Locate every blood parasite and identify its species.
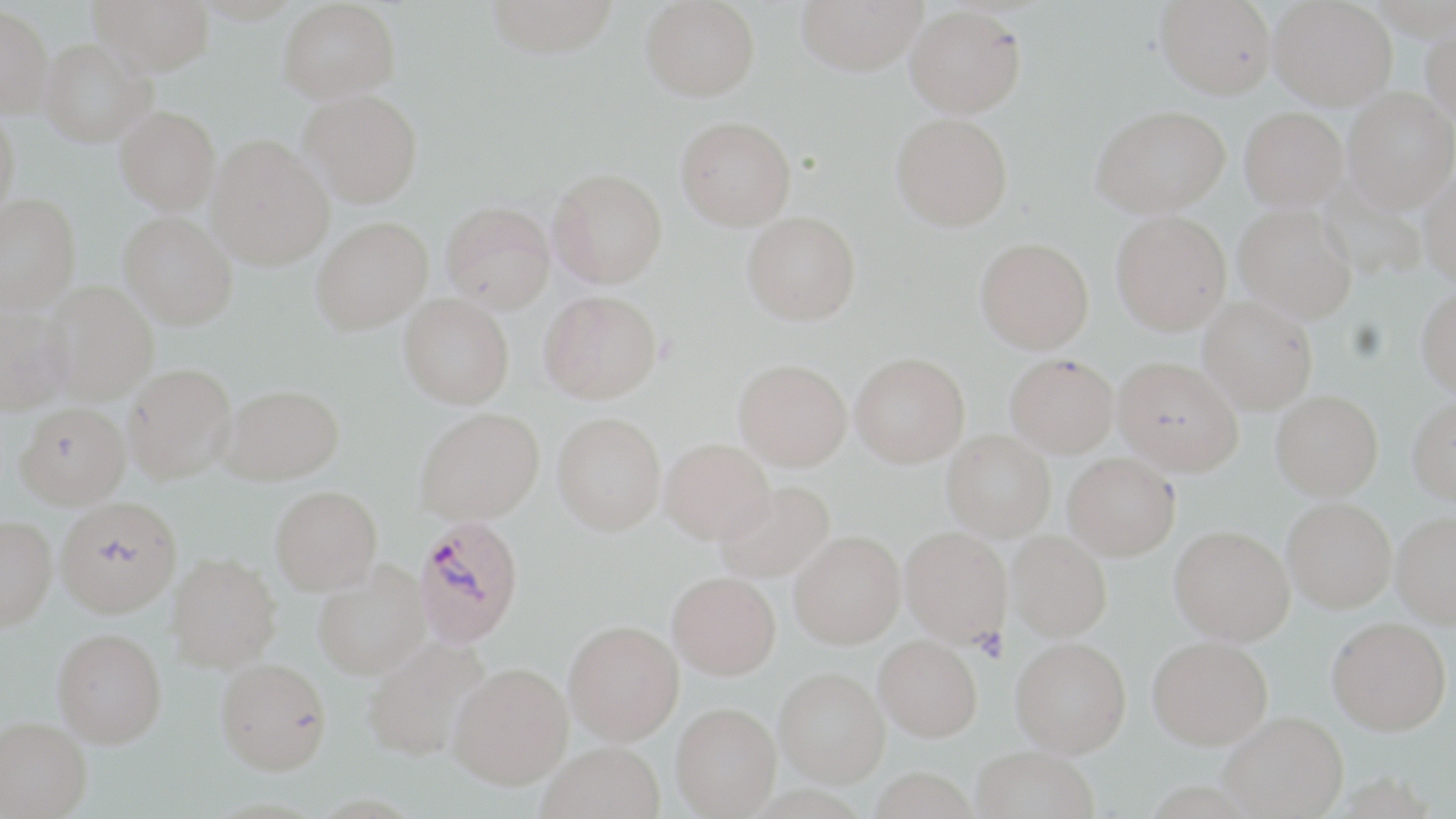

Approximate bounding boxes as (x1, y1, x2, y2) in pixels.
Plasmodium falciparum-infected red blood cells: (414, 515, 524, 648).
No Plasmodium ovale, Plasmodium malariae, Plasmodium vivax, Babesia divergens, or Trypanosoma brucei observed.

slide_level_diagnosis: Plasmodium falciparum
image_size: 1456×819 pixels
platelet_locations: 'approximate bounding boxes as (x1, y1, x2, y2) in pixels: (972, 627, 1009, 664)'
stain: May-Grünwald-Giemsa
uninfected_red_blood_cell_locations: 'approximate bounding boxes as (x1, y1, x2, y2) in pixels: (90, 0, 215, 76), (485, 0, 620, 57), (640, 0, 760, 101), (796, 0, 926, 75), (1156, 0, 1276, 99), (1269, 0, 1397, 109), (278, 1, 401, 102), (0, 3, 53, 116), (905, 5, 1027, 118), (1422, 20, 1456, 127), (40, 38, 155, 146), (299, 89, 422, 207), (1343, 89, 1456, 211), (1091, 105, 1230, 217), (115, 106, 220, 215), (1240, 106, 1347, 210), (0, 108, 20, 221), (891, 112, 1013, 231), (676, 115, 796, 230), (206, 135, 334, 270), (548, 168, 667, 288), (1418, 169, 1456, 285), (1318, 181, 1425, 280), (0, 194, 80, 311), (441, 201, 555, 312), (1234, 204, 1357, 322), (741, 211, 861, 325), (1110, 211, 1231, 334), (119, 212, 238, 329), (311, 217, 432, 334), (975, 237, 1094, 353), (44, 281, 159, 405), (1416, 286, 1456, 396), (539, 290, 663, 403), (399, 294, 514, 408), (1199, 296, 1317, 413), (0, 301, 72, 415), (850, 352, 969, 467), (1005, 353, 1119, 457), (1113, 356, 1242, 474), (734, 358, 852, 470), (122, 363, 237, 483), (220, 384, 344, 484), (1270, 390, 1383, 500), (1407, 396, 1456, 506), (15, 402, 131, 509), (415, 408, 544, 524), (553, 412, 666, 535), (941, 430, 1055, 540), (661, 437, 774, 542), (1063, 452, 1180, 559), (713, 480, 835, 583), (270, 485, 383, 594), (1282, 497, 1396, 612), (55, 498, 182, 618), (1390, 511, 1456, 627), (0, 516, 57, 630), (1169, 525, 1294, 644), (900, 526, 1012, 645), (789, 531, 906, 648), (1007, 531, 1112, 641), (167, 553, 281, 672), (313, 562, 430, 680), (667, 571, 780, 679), (1327, 617, 1451, 735), (564, 620, 684, 744), (52, 628, 167, 747), (874, 635, 981, 740), (1147, 635, 1273, 748), (361, 636, 491, 762), (1010, 638, 1131, 757), (215, 658, 332, 774), (448, 662, 572, 788), (775, 667, 889, 787), (671, 702, 781, 816), (1220, 712, 1348, 818), (0, 717, 91, 818), (538, 742, 665, 819), (970, 746, 1098, 819), (868, 769, 980, 819)'
magnification: 1000x
modality: optical microscopy
field_of_view: single
preparation: thin blood smear